Outline platelets.
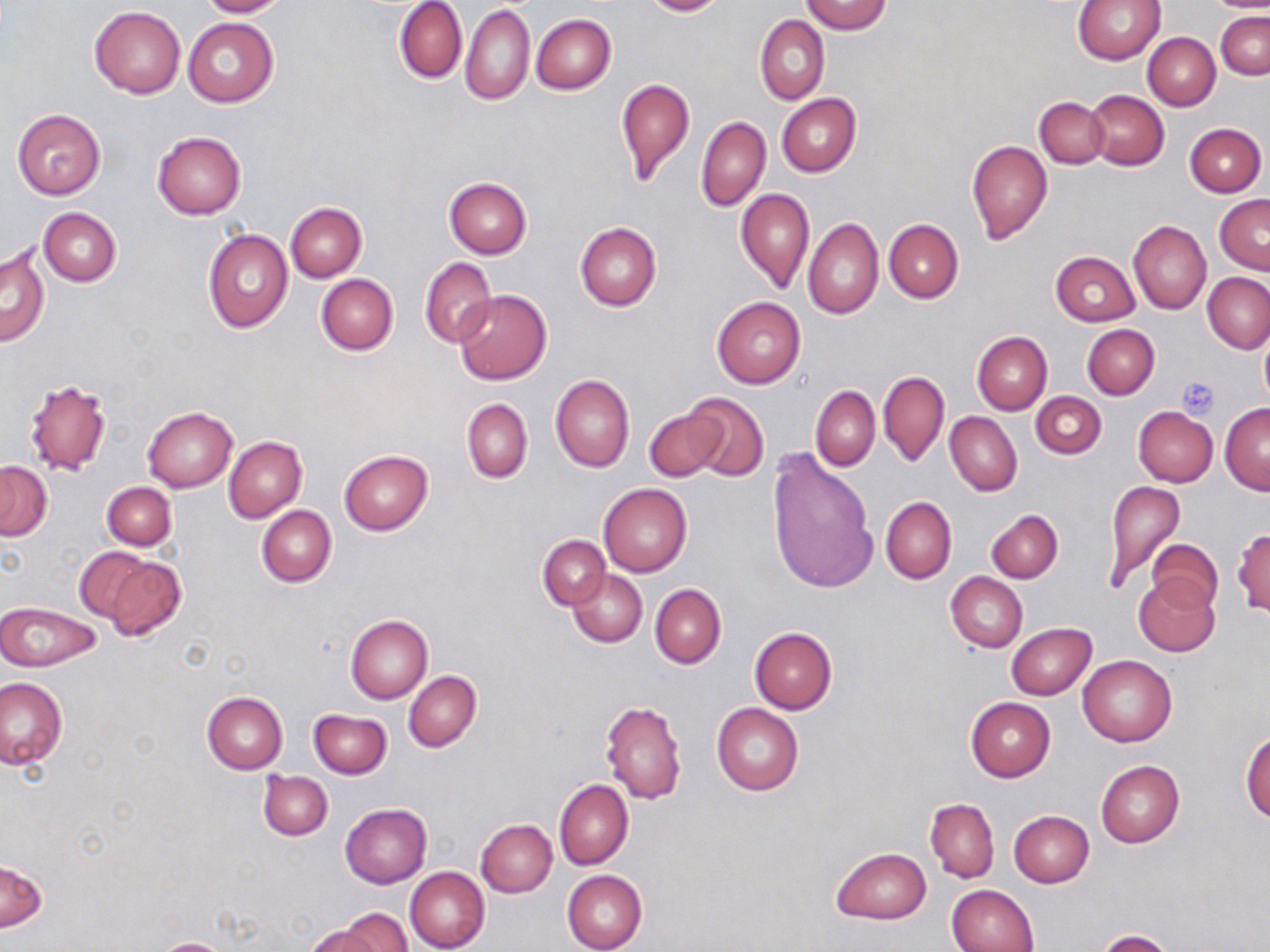

Approximate bounding boxes as [x1, y1, x2, y2] in pixels.
Platelets: [1176, 379, 1218, 419].

slide_level_diagnosis: no evidence of blood parasites
field_of_view: single
magnification: 1000x
image_size: 1270×952 pixels
stain: May-Grünwald-Giemsa
modality: optical microscopy
preparation: thin blood smear
uninfected_red_blood_cell_locations: 'approximate bounding boxes as [x1, y1, x2, y2] in pixels: [197, 0, 290, 17], [395, 0, 467, 84], [641, 0, 729, 16], [800, 0, 891, 34], [1072, 0, 1166, 65], [1205, 1, 1270, 12], [461, 5, 536, 106], [89, 7, 186, 97], [1216, 10, 1269, 80], [754, 14, 829, 105], [532, 15, 615, 94], [182, 17, 279, 107], [1143, 32, 1221, 110], [615, 77, 695, 185], [1086, 89, 1169, 169], [777, 93, 861, 177], [1035, 97, 1108, 168], [11, 109, 106, 199], [696, 114, 770, 211], [1185, 122, 1266, 196], [151, 131, 247, 220], [967, 141, 1052, 245], [443, 178, 531, 259], [735, 188, 814, 293], [1214, 195, 1270, 274], [284, 202, 367, 282], [39, 208, 121, 286], [803, 218, 884, 319], [884, 219, 963, 303], [1129, 220, 1211, 315], [574, 222, 662, 310], [203, 228, 292, 333], [1, 247, 50, 347], [1051, 250, 1140, 325], [420, 258, 497, 348], [1203, 272, 1270, 353], [316, 274, 398, 355], [453, 290, 552, 384], [712, 297, 806, 388], [1083, 324, 1160, 399], [1258, 328, 1270, 408], [972, 332, 1051, 415], [878, 370, 949, 468], [551, 374, 634, 473], [24, 377, 112, 477], [811, 386, 880, 471], [1031, 391, 1106, 459], [682, 392, 769, 483], [461, 399, 533, 484], [1219, 404, 1270, 492], [143, 406, 237, 492], [644, 406, 727, 481], [1134, 407, 1217, 487], [945, 412, 1022, 496], [224, 436, 306, 523], [766, 447, 876, 595], [339, 449, 432, 535], [0, 461, 51, 540], [1104, 481, 1184, 588], [102, 482, 176, 550], [599, 483, 691, 576], [880, 496, 955, 585], [256, 504, 336, 587], [987, 509, 1063, 583], [1233, 528, 1270, 617], [538, 535, 610, 610], [1146, 537, 1223, 614], [97, 552, 186, 641], [568, 569, 647, 647], [946, 572, 1027, 652], [1133, 574, 1220, 657], [650, 584, 726, 668], [0, 601, 101, 672], [345, 615, 432, 703], [1006, 623, 1096, 699], [751, 627, 837, 714], [1078, 654, 1177, 746], [404, 670, 481, 752], [0, 678, 66, 770], [201, 691, 288, 775], [965, 697, 1055, 781], [600, 700, 687, 805], [712, 704, 804, 796], [309, 709, 390, 778], [1241, 729, 1270, 821], [1095, 760, 1184, 848], [258, 770, 333, 841], [554, 779, 633, 870], [925, 797, 999, 883], [339, 803, 431, 889], [1008, 810, 1094, 887], [476, 820, 556, 897], [832, 847, 931, 923], [0, 860, 48, 933], [405, 867, 489, 952], [562, 870, 648, 952], [945, 885, 1039, 952], [334, 912, 414, 952], [306, 926, 381, 952], [1097, 930, 1174, 952], [151, 938, 235, 952]'